Report the malaria status of this cell.
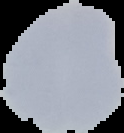
Uninfected.

Cell region segmented out of the field of view; the surrounding area is masked to black. Image is 124×133 pixels. From a thin blood film.